Comment on the morphology of the red blood cells.
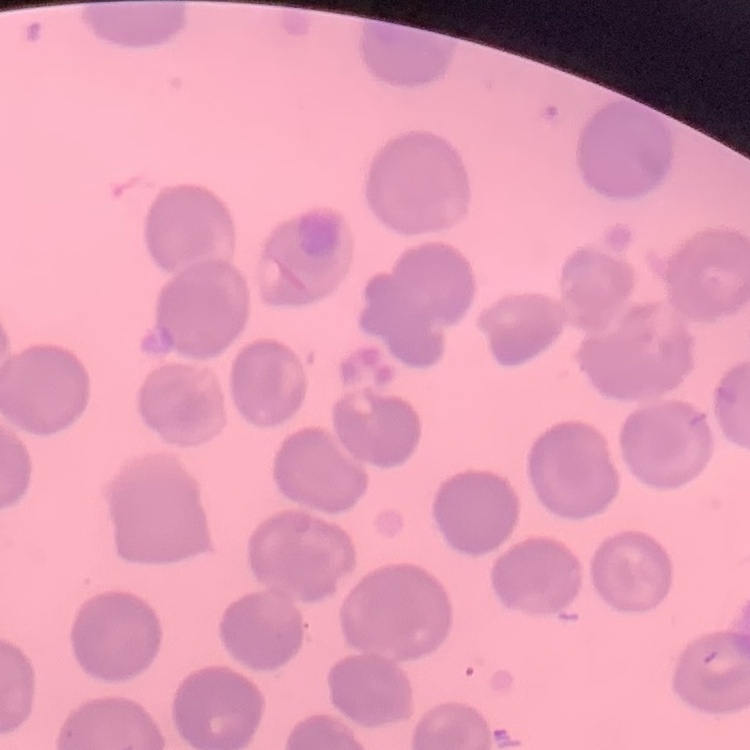

They show no rouleaux formation.

stain: Field's or Giemsa
preparation: thin blood smear
image_type: square crop of a larger photomicrograph